Locate every uninfected red blood cell.
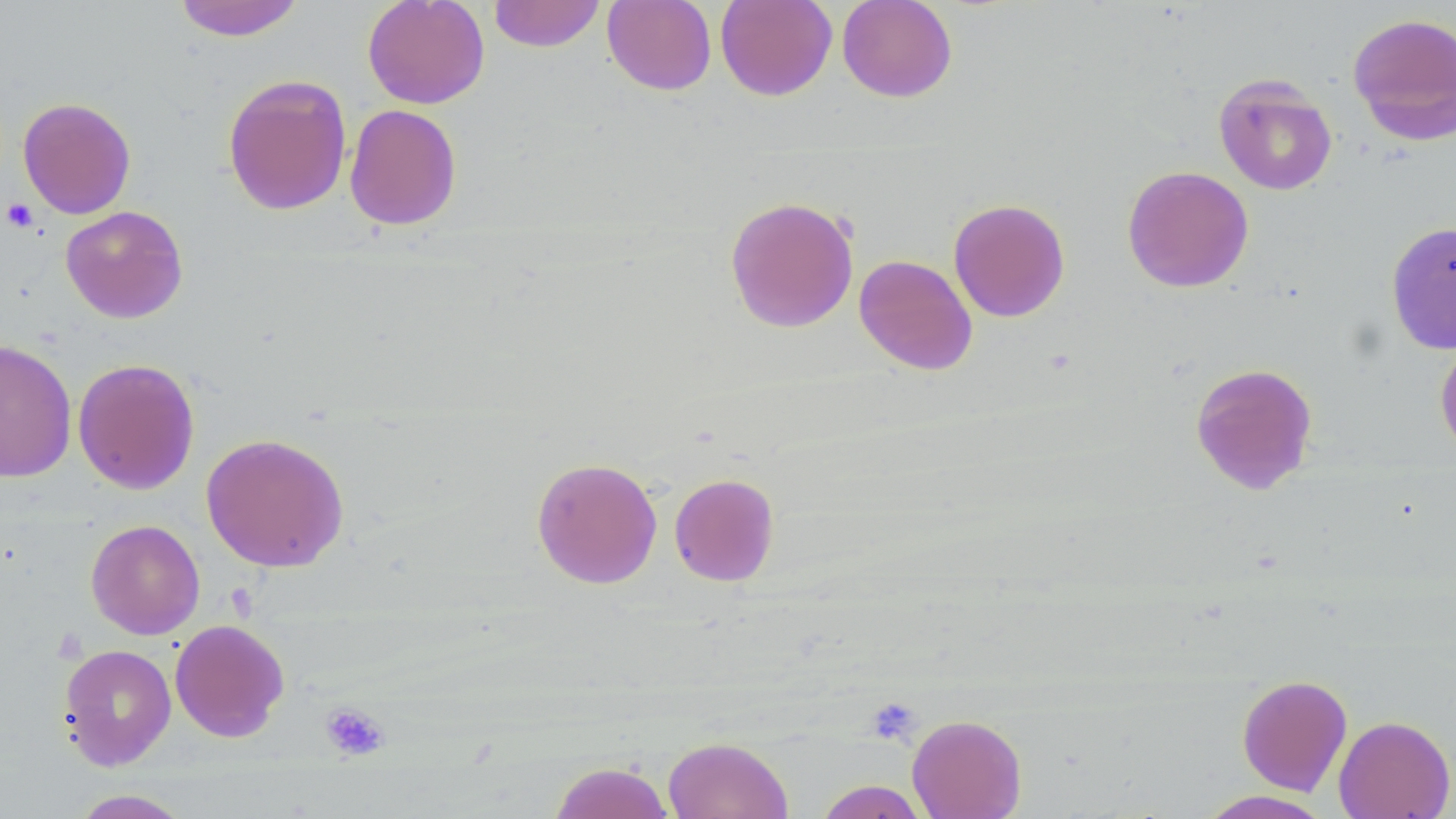
Approximate bounding boxes as (x1,y1)-(x2,y2) corner pairs in pixels.
Uninfected red blood cells: (172,0)-(306,41), (362,0)-(490,109), (488,0)-(606,52), (602,0)-(717,96), (715,0)-(837,101), (837,0)-(958,102), (1347,11)-(1456,146), (221,73)-(352,216), (1213,73)-(1338,196), (17,97)-(136,219), (344,103)-(462,231), (1122,165)-(1254,293), (724,195)-(859,334), (948,198)-(1071,323), (60,205)-(188,323), (1385,221)-(1456,354), (854,254)-(978,375), (1434,332)-(1456,461), (0,339)-(77,483), (72,357)-(200,495), (1190,362)-(1318,495), (200,432)-(350,573), (531,457)-(663,589), (669,473)-(780,586), (85,519)-(205,640), (169,619)-(290,742), (58,643)-(176,770), (1237,674)-(1353,796), (907,714)-(1027,819), (1333,714)-(1455,818), (662,736)-(794,819), (548,760)-(676,819), (814,779)-(931,819), (68,789)-(193,818), (1194,789)-(1335,819).

Platelet locations: (2,197)-(39,232), (865,697)-(922,746), (320,701)-(390,761). Slide-level diagnosis: no evidence of blood parasites. Optical microscopy. Thin blood smear. May-Grünwald-Giemsa-stained preparation. 1000x magnification. Image is 1456×819 pixels. Single field of view.